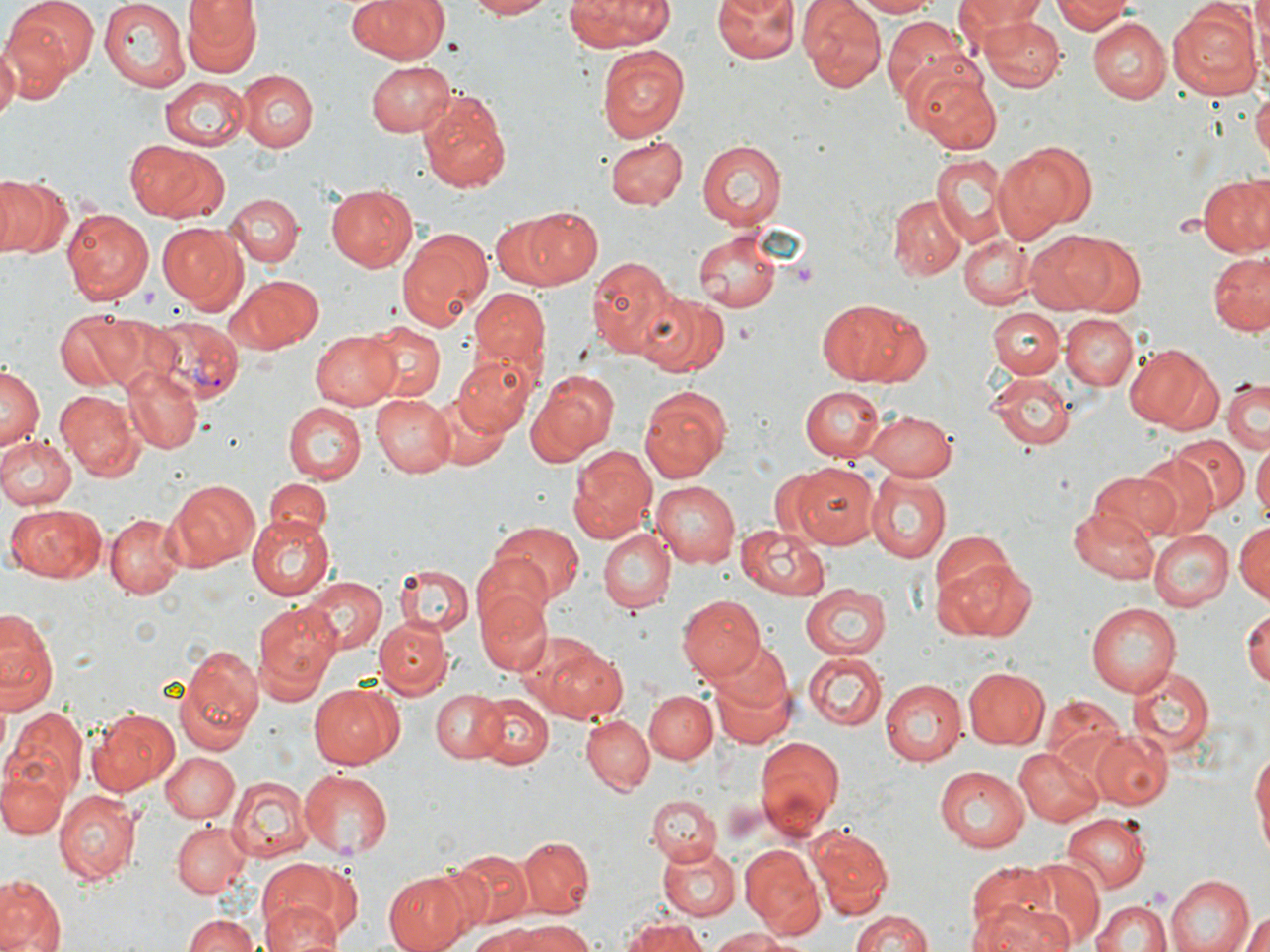
slide-level diagnosis = Plasmodium vivax
modality = light microscopy
platelet locations = approximate bounding boxes as (x1,y1)-(x2,y2) corner pairs in pixels: (791,261)-(818,282), (1143,887)-(1172,910)
uninfected red blood cell locations = approximate bounding boxes as (x1,y1)-(x2,y2) corner pairs in pixels: (6,0)-(97,79), (99,0)-(191,91), (182,0)-(259,75), (346,0)-(448,65), (461,0)-(553,19), (563,0)-(675,50), (712,0)-(800,63), (850,0)-(943,17), (958,0)-(1051,47), (1051,0)-(1131,36), (1245,0)-(1268,74), (1255,0)-(1270,62), (800,2)-(884,91), (1167,4)-(1259,101), (576,11)-(678,116), (883,15)-(973,103), (978,17)-(1065,92), (1089,20)-(1171,103), (2,37)-(52,111), (0,41)-(20,123), (598,44)-(688,141), (365,59)-(455,137), (904,60)-(1004,156), (235,68)-(318,152), (161,77)-(251,151), (1252,82)-(1270,171), (418,88)-(513,193), (604,136)-(685,209), (127,140)-(227,222), (697,140)-(785,228), (994,141)-(1095,242), (931,153)-(1009,248), (0,176)-(70,260), (1198,177)-(1270,257), (326,184)-(417,271), (223,192)-(302,267), (890,194)-(966,278), (501,206)-(601,289), (61,207)-(153,303), (156,222)-(245,308), (395,226)-(492,332), (695,231)-(782,312), (1026,232)-(1119,312), (960,235)-(1037,307), (1064,235)-(1146,313), (1209,252)-(1270,335), (584,254)-(681,361), (227,274)-(320,354), (470,288)-(548,377), (640,292)-(732,377), (815,299)-(928,387), (991,308)-(1064,378), (56,310)-(148,391), (1062,316)-(1137,391), (359,320)-(446,404), (310,329)-(403,410), (1124,344)-(1222,431), (454,354)-(536,434), (0,365)-(42,455), (123,365)-(204,455), (526,369)-(618,465), (986,372)-(1076,450), (1223,377)-(1268,453), (638,385)-(734,482), (801,385)-(885,461), (54,391)-(139,479), (373,392)-(458,476), (428,395)-(509,471), (282,402)-(366,484), (865,411)-(956,481), (0,433)-(76,509), (1169,436)-(1248,512), (1252,445)-(1269,528), (567,446)-(656,543), (1132,455)-(1216,537), (791,462)-(879,547), (866,471)-(950,563), (1090,471)-(1181,539), (166,479)-(260,571), (264,480)-(330,536), (651,481)-(740,567), (6,504)-(106,583), (1070,507)-(1158,584), (105,514)-(186,598), (248,517)-(335,602), (488,520)-(585,607), (1235,521)-(1268,603), (737,523)-(833,598), (1193,524)-(1268,607), (598,528)-(676,612), (1149,530)-(1232,612), (933,532)-(1015,604), (469,555)-(557,638), (939,557)-(1037,641), (396,563)-(472,634), (300,576)-(387,655), (801,583)-(893,658), (475,584)-(550,677), (678,595)-(766,679), (255,601)-(343,694), (1086,601)-(1182,697), (1243,606)-(1269,692), (0,610)-(58,712), (375,618)-(450,698), (530,640)-(628,724), (708,649)-(796,751), (804,652)-(887,730), (172,655)-(262,754), (1128,665)-(1215,758), (961,666)-(1050,750), (880,678)-(964,766), (308,683)-(403,768), (430,689)-(506,763), (645,690)-(716,764), (475,692)-(556,769), (1042,697)-(1130,781), (4,705)-(88,805), (87,707)-(179,797), (582,716)-(652,793), (1093,729)-(1174,807), (755,736)-(845,836), (1249,745)-(1270,862), (1014,746)-(1100,825), (160,752)-(239,822), (1,764)-(67,840), (933,766)-(1029,852), (296,768)-(395,858), (228,775)-(310,862), (236,775)-(323,934), (56,791)-(138,882), (648,793)-(721,866), (1061,813)-(1151,895), (171,822)-(251,898), (809,825)-(892,916), (519,837)-(594,917), (656,843)-(740,919), (739,844)-(825,938), (453,850)-(534,927), (1018,857)-(1104,943), (257,860)-(352,941), (966,861)-(1056,939), (382,868)-(475,952), (1165,874)-(1254,952), (0,875)-(65,951), (1091,891)-(1248,952), (972,898)-(1076,952), (1092,898)-(1169,952), (262,901)-(344,951), (847,907)-(935,952), (1238,911)-(1270,952), (181,913)-(261,952), (619,915)-(709,952), (498,919)-(592,952), (707,927)-(800,951), (462,928)-(545,952)
image size = 1270×952 pixels
magnification = 1000x
Plasmodium vivax-infected red blood cell locations = approximate bounding boxes as (x1,y1)-(x2,y2) corner pairs in pixels: (147,317)-(243,403)
stain = May-Grünwald-Giemsa
preparation = thin blood smear
field of view = single